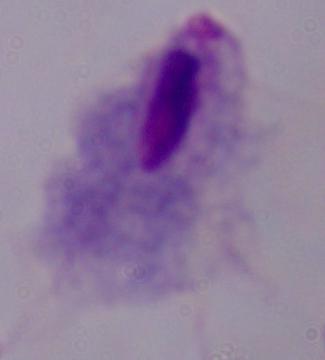
Summary:
  - Identification: trichomonad
  - Magnification: 1000x
  - Modality: micrograph